Comment on the morphology of the erythrocytes.
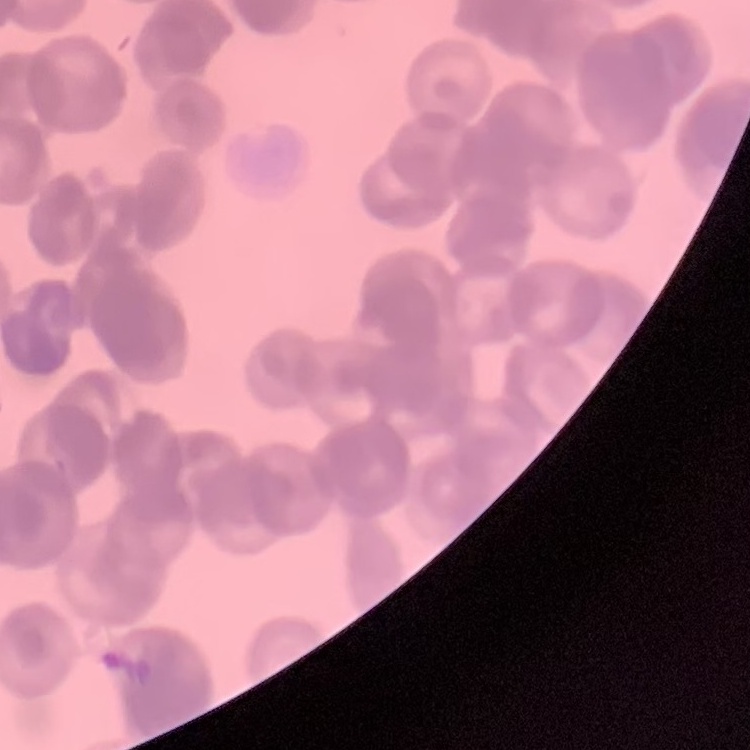
They show rouleaux formation.

Stained with either Field's or Giemsa. Square crop of a larger photomicrograph. Thin blood film.